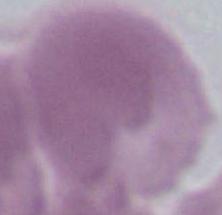

Summary:
  - Modality: micrograph
  - Identification: red blood cell
  - Magnification: 1000x